Classify this cell by malaria status.
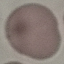
It is uninfected.

Summary:
  - Capture: smartphone through the microscope eyepiece
  - Preparation: thin blood film
  - Image type: automatically extracted cell patch, resized to 64 × 64 pixels
  - Stain: Giemsa